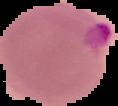
image size = 118×106 pixels
image type = segmented cell region on a black background
malaria status = parasitized
preparation = thin blood film